Locate every Trypanosoma brucei.
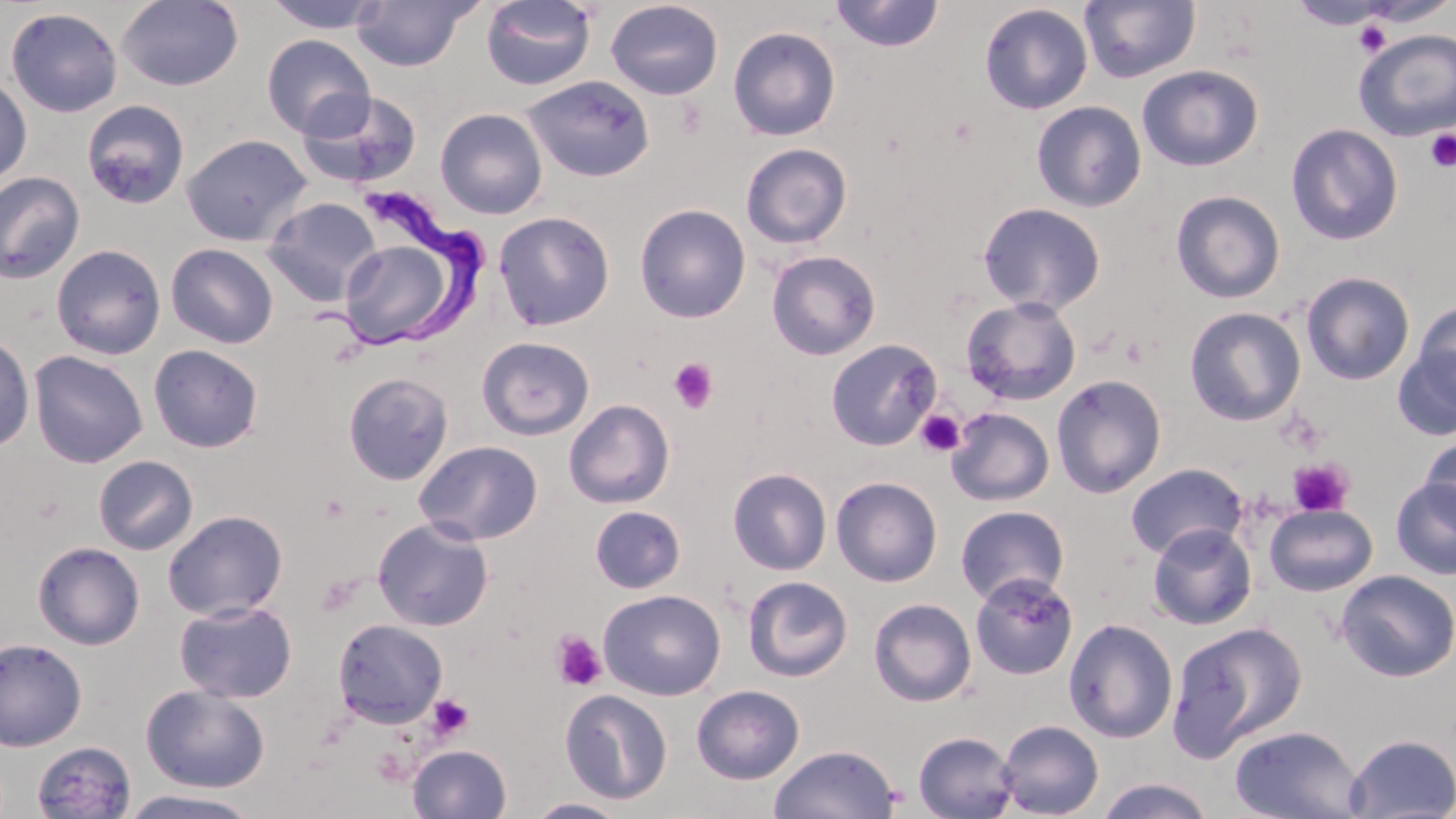
Approximate bounding boxes as named x1/y1/x2/y2 corners in pixels.
Trypanosoma brucei: (x1=308, y1=188, x2=495, y2=356).

slide-level diagnosis = Trypanosoma brucei
modality = optical microscopy
preparation = thin blood smear
platelet locations = approximate bounding boxes as named x1/y1/x2/y2 corners in pixels: (x1=1352, y1=20, x2=1394, y2=57), (x1=1425, y1=128, x2=1456, y2=172), (x1=667, y1=358, x2=719, y2=414), (x1=915, y1=410, x2=965, y2=458), (x1=1288, y1=458, x2=1354, y2=517), (x1=551, y1=630, x2=607, y2=692), (x1=427, y1=695, x2=473, y2=741), (x1=371, y1=748, x2=413, y2=787)
image size = 1456×819 pixels
stain = May-Grünwald-Giemsa
field of view = one of a larger specimen
magnification = 1000x
uninfected red blood cell locations = approximate bounding boxes as named x1/y1/x2/y2 corners in pixels: (x1=117, y1=0, x2=243, y2=91), (x1=261, y1=0, x2=390, y2=33), (x1=350, y1=0, x2=480, y2=72), (x1=1079, y1=0, x2=1200, y2=84), (x1=481, y1=1, x2=597, y2=90), (x1=605, y1=1, x2=724, y2=100), (x1=829, y1=1, x2=945, y2=52), (x1=1288, y1=1, x2=1394, y2=30), (x1=978, y1=3, x2=1093, y2=115), (x1=5, y1=7, x2=123, y2=117), (x1=728, y1=26, x2=840, y2=141), (x1=1353, y1=28, x2=1456, y2=141), (x1=261, y1=34, x2=375, y2=139), (x1=1137, y1=64, x2=1263, y2=171), (x1=0, y1=75, x2=32, y2=189), (x1=522, y1=75, x2=655, y2=182), (x1=297, y1=89, x2=423, y2=190), (x1=81, y1=100, x2=190, y2=209), (x1=1031, y1=101, x2=1147, y2=212), (x1=435, y1=108, x2=547, y2=219), (x1=1285, y1=123, x2=1404, y2=246), (x1=181, y1=133, x2=312, y2=247), (x1=741, y1=143, x2=852, y2=249), (x1=0, y1=172, x2=86, y2=284), (x1=1170, y1=190, x2=1285, y2=303), (x1=263, y1=196, x2=382, y2=306), (x1=977, y1=201, x2=1105, y2=314), (x1=634, y1=204, x2=751, y2=323), (x1=493, y1=211, x2=615, y2=331), (x1=337, y1=234, x2=464, y2=350), (x1=166, y1=243, x2=279, y2=349), (x1=51, y1=244, x2=166, y2=360), (x1=766, y1=250, x2=881, y2=360), (x1=1301, y1=271, x2=1415, y2=385), (x1=961, y1=296, x2=1082, y2=405), (x1=1412, y1=299, x2=1456, y2=407), (x1=1184, y1=306, x2=1306, y2=426), (x1=0, y1=334, x2=35, y2=452), (x1=477, y1=336, x2=595, y2=440), (x1=826, y1=339, x2=941, y2=451), (x1=148, y1=344, x2=263, y2=453), (x1=1392, y1=346, x2=1456, y2=442), (x1=28, y1=350, x2=148, y2=468), (x1=343, y1=372, x2=453, y2=486), (x1=1050, y1=374, x2=1167, y2=498), (x1=563, y1=399, x2=674, y2=508), (x1=945, y1=407, x2=1055, y2=506), (x1=1418, y1=435, x2=1455, y2=528), (x1=413, y1=440, x2=543, y2=546), (x1=92, y1=455, x2=198, y2=555), (x1=1125, y1=463, x2=1248, y2=560), (x1=727, y1=468, x2=832, y2=575), (x1=831, y1=476, x2=943, y2=587), (x1=1391, y1=477, x2=1456, y2=579), (x1=1264, y1=503, x2=1377, y2=596), (x1=590, y1=505, x2=686, y2=593), (x1=955, y1=505, x2=1069, y2=606), (x1=162, y1=509, x2=288, y2=620), (x1=373, y1=517, x2=494, y2=632), (x1=1147, y1=523, x2=1257, y2=630), (x1=32, y1=541, x2=145, y2=650), (x1=1336, y1=570, x2=1456, y2=682), (x1=970, y1=572, x2=1078, y2=680), (x1=743, y1=576, x2=853, y2=681), (x1=599, y1=589, x2=725, y2=700), (x1=868, y1=597, x2=977, y2=707), (x1=174, y1=599, x2=297, y2=703), (x1=332, y1=618, x2=448, y2=729), (x1=1063, y1=618, x2=1178, y2=743), (x1=1168, y1=620, x2=1308, y2=759), (x1=0, y1=637, x2=87, y2=751), (x1=141, y1=684, x2=270, y2=794), (x1=691, y1=684, x2=805, y2=784), (x1=560, y1=689, x2=673, y2=805), (x1=996, y1=719, x2=1103, y2=818), (x1=1228, y1=724, x2=1365, y2=819), (x1=913, y1=731, x2=1020, y2=818), (x1=1344, y1=734, x2=1456, y2=818), (x1=31, y1=741, x2=137, y2=819), (x1=407, y1=744, x2=512, y2=818), (x1=768, y1=744, x2=900, y2=819), (x1=1094, y1=777, x2=1216, y2=819), (x1=118, y1=789, x2=263, y2=818), (x1=523, y1=797, x2=633, y2=818)